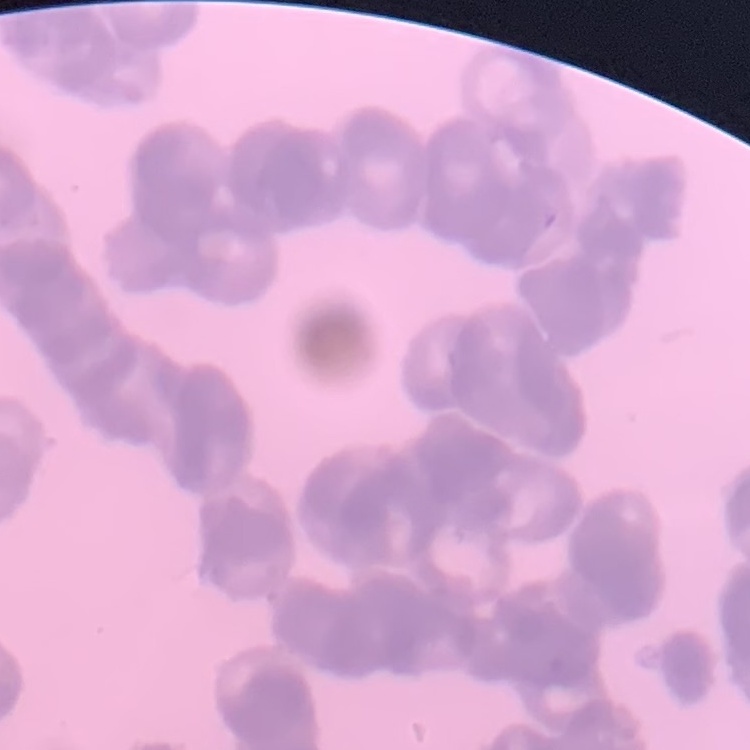
The erythrocytes show rouleaux formation. Square crop of a larger photomicrograph. Stained with either Field's or Giemsa. Thin blood film.